Classify this cell by malaria status.
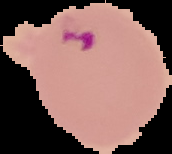

It is parasitized.

From a thin blood smear. The area outside the segmented cell region is set to black. Image is 172×154 pixels.